Identify the preparation type.
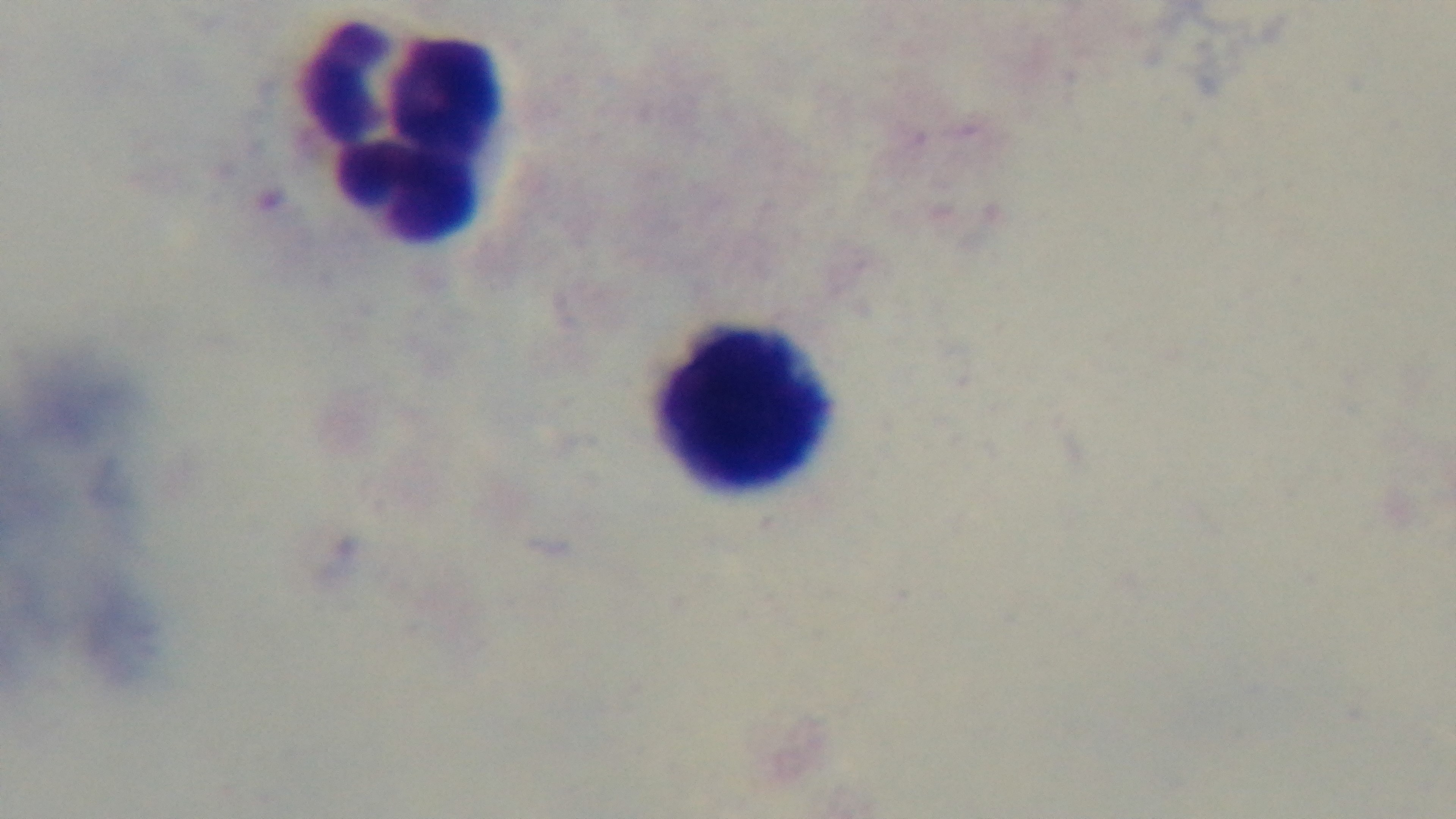

It is a thick blood film.

Oil-immersion objective, 100x. Malaria status: uninfected. Giemsa-stained. One field from the slide. Mounted 4K digital camera. Light microscopy.